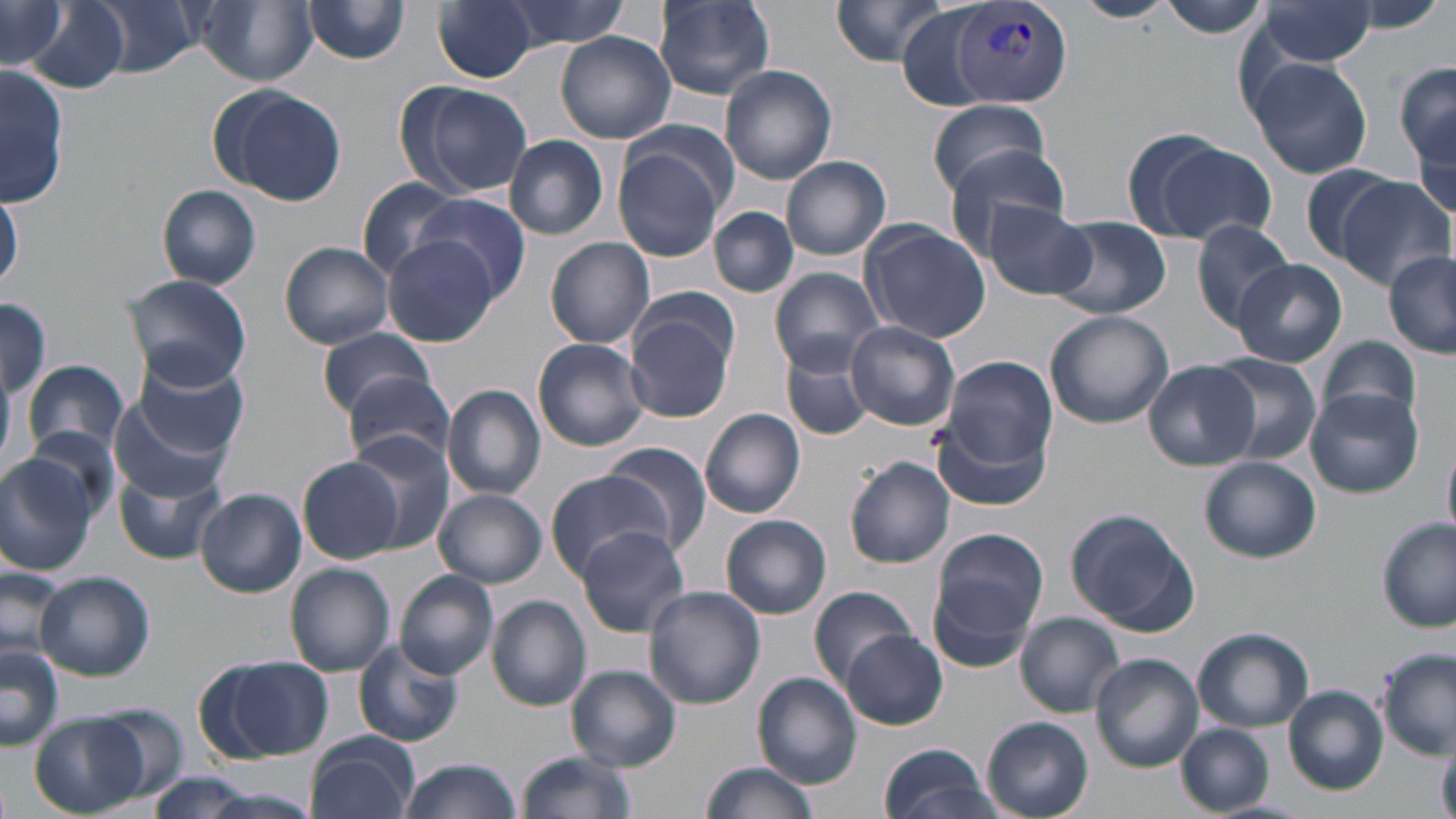
slide-level diagnosis = Plasmodium vivax
magnification = 1000x
uninfected red blood cell locations = approximate bounding boxes as [x1, y1, x2, y2] in pixels: [85, 0, 202, 77], [301, 0, 413, 65], [432, 0, 541, 84], [491, 0, 633, 52], [828, 0, 956, 68], [1075, 0, 1174, 22], [1158, 0, 1277, 40], [2, 1, 67, 70], [655, 1, 775, 99], [25, 2, 133, 96], [190, 2, 320, 85], [1252, 2, 1382, 68], [893, 4, 996, 109], [557, 32, 675, 143], [1248, 57, 1374, 180], [3, 61, 68, 211], [1395, 61, 1456, 168], [719, 65, 837, 184], [404, 82, 532, 198], [212, 85, 348, 205], [927, 98, 1049, 199], [1409, 109, 1456, 230], [624, 117, 741, 217], [503, 134, 609, 239], [1136, 137, 1277, 246], [943, 145, 1075, 255], [613, 146, 725, 261], [781, 155, 892, 260], [1299, 163, 1402, 264], [1333, 177, 1455, 291], [355, 179, 468, 280], [157, 184, 262, 290], [0, 187, 22, 294], [415, 193, 532, 302], [984, 199, 1095, 300], [711, 207, 798, 297], [1049, 215, 1170, 319], [1191, 219, 1295, 328], [860, 221, 991, 344], [378, 236, 501, 347], [546, 236, 655, 349], [280, 241, 395, 349], [1383, 252, 1455, 358], [1230, 258, 1346, 367], [769, 266, 883, 375], [122, 275, 251, 391], [0, 297, 51, 401], [626, 305, 738, 425], [1044, 310, 1174, 429], [846, 321, 959, 431], [316, 327, 434, 417], [1318, 337, 1423, 433], [531, 338, 652, 451], [779, 346, 872, 442], [132, 353, 252, 461], [1205, 355, 1321, 462], [938, 357, 1058, 475], [1143, 358, 1260, 470], [25, 361, 129, 457], [344, 370, 457, 467], [444, 384, 547, 499], [1306, 390, 1423, 498], [107, 396, 234, 505], [699, 408, 806, 518], [933, 414, 1052, 513], [24, 424, 122, 521], [349, 433, 458, 553], [599, 442, 713, 556], [1443, 449, 1455, 541], [0, 455, 95, 577], [845, 456, 956, 568], [1200, 456, 1321, 563], [297, 457, 407, 564], [115, 465, 225, 564], [543, 472, 671, 580], [196, 489, 305, 597], [434, 490, 546, 587], [1065, 508, 1200, 635], [722, 515, 832, 619], [1377, 517, 1455, 632], [574, 526, 691, 637], [931, 526, 1049, 643], [0, 564, 70, 667], [285, 564, 396, 676], [395, 570, 498, 681], [36, 572, 155, 682], [643, 586, 764, 710], [808, 586, 920, 689], [486, 595, 592, 711], [1016, 613, 1126, 716], [1192, 626, 1313, 732], [844, 630, 947, 729], [356, 640, 465, 747], [0, 644, 63, 750], [1378, 651, 1454, 758], [1092, 653, 1203, 772], [202, 655, 333, 763], [569, 665, 682, 770], [753, 671, 861, 788], [1283, 685, 1388, 795], [70, 706, 187, 805], [30, 714, 149, 815], [982, 716, 1094, 819], [1176, 724, 1275, 814], [306, 735, 421, 819], [878, 740, 999, 819], [516, 750, 635, 819], [396, 758, 520, 819], [700, 760, 817, 819], [135, 773, 273, 817]
preparation = thin blood film
image size = 1456×819 pixels
stain = May-Grünwald-Giemsa
modality = optical microscopy
field of view = single
Plasmodium vivax-infected red blood cell locations = approximate bounding boxes as [x1, y1, x2, y2] in pixels: [951, 4, 1072, 108]